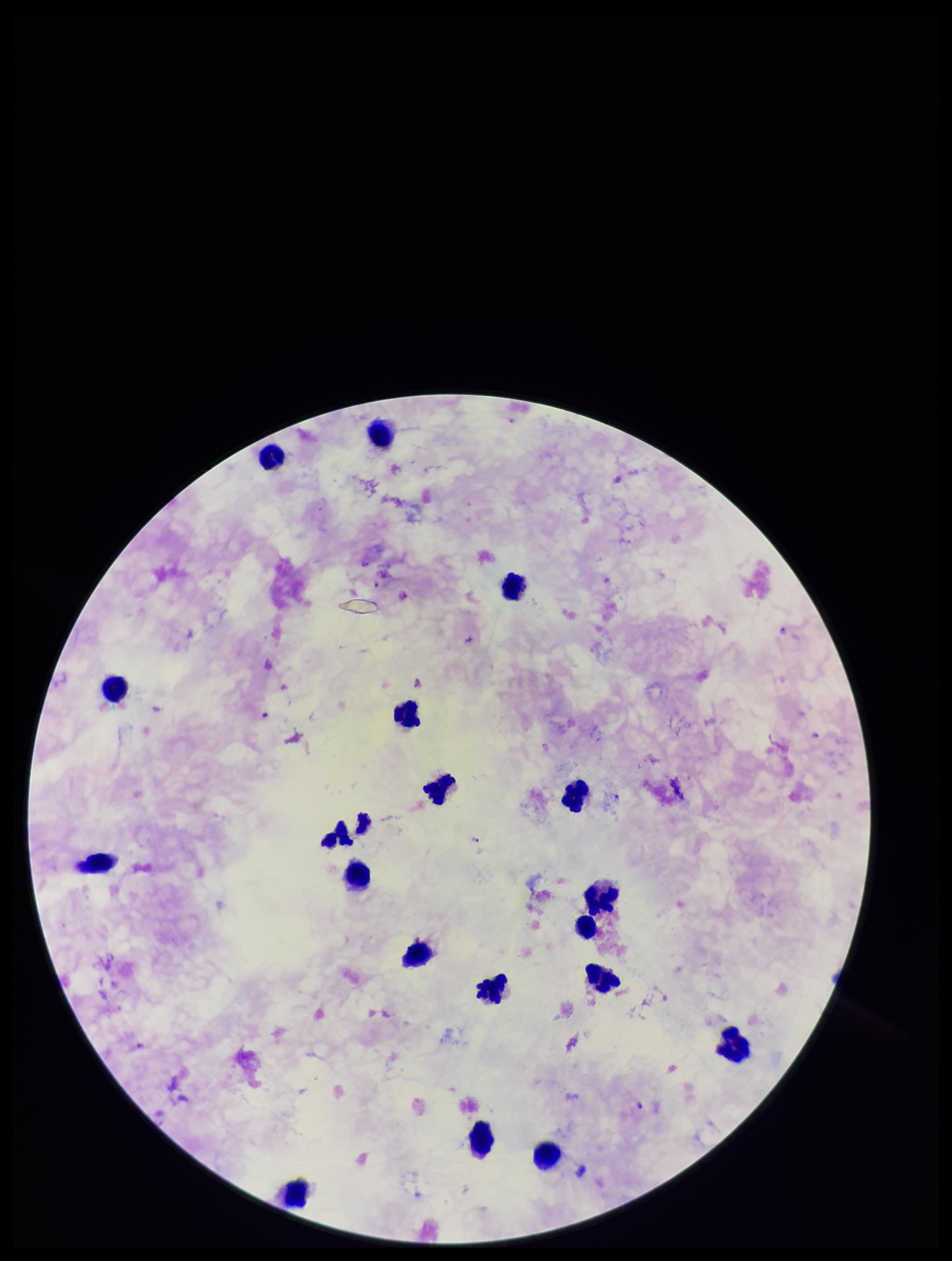

patient_malaria_status: positive
preparation: thick blood smear
field_of_view: one from this slide
capture: smartphone photograph through the microscope eyepiece
species_reported_for_this_patient: Plasmodium falciparum
image_size: 952×1261 pixels
plasmodium_parasites: detected
stain: Giemsa
parasite_count: 5
leukocyte_count: 19